Find each white blood cell.
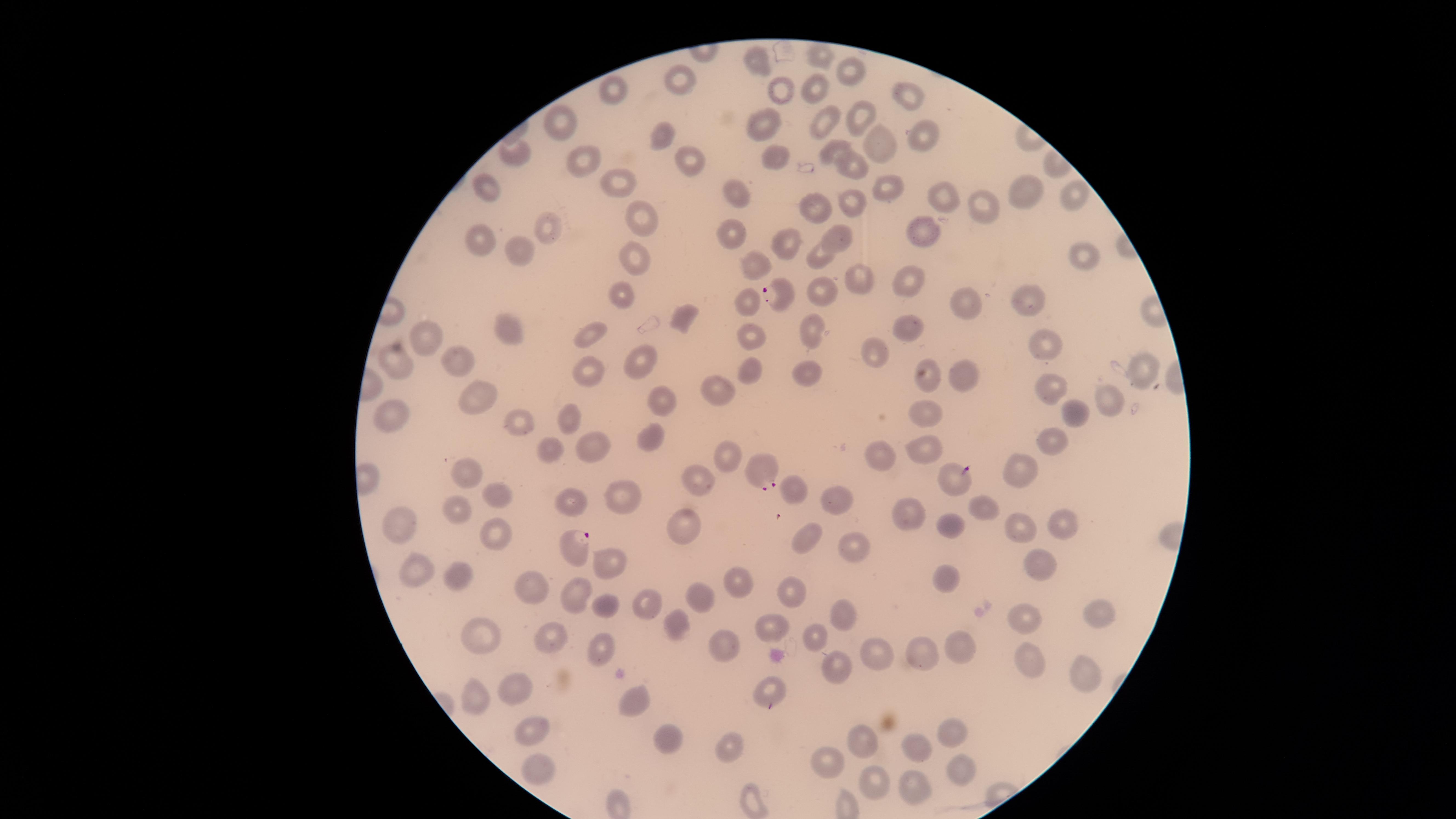
No white blood cells identified.

visible region = circular
species = Plasmodium falciparum
uninfected red blood cells = approximate marker points, in pixels from the top-left corner: (x=817, y=54), (x=759, y=62), (x=848, y=67), (x=682, y=82), (x=818, y=88), (x=613, y=90), (x=777, y=90), (x=910, y=90), (x=861, y=113), (x=567, y=116), (x=825, y=118), (x=768, y=124), (x=661, y=132), (x=922, y=138), (x=877, y=146), (x=831, y=147), (x=520, y=155), (x=772, y=155), (x=576, y=161), (x=686, y=162), (x=846, y=166), (x=610, y=180), (x=483, y=186), (x=890, y=190), (x=1020, y=192), (x=941, y=195), (x=1078, y=196), (x=744, y=201), (x=978, y=203), (x=815, y=204), (x=857, y=204), (x=643, y=216), (x=548, y=226), (x=730, y=230), (x=837, y=236), (x=485, y=238), (x=920, y=241), (x=788, y=244), (x=523, y=249), (x=823, y=254), (x=1080, y=256), (x=632, y=261), (x=758, y=262), (x=861, y=279), (x=906, y=281), (x=823, y=292), (x=624, y=296), (x=1024, y=298), (x=967, y=302), (x=748, y=303), (x=687, y=318), (x=817, y=326), (x=507, y=327), (x=590, y=330), (x=906, y=331), (x=425, y=332), (x=756, y=339), (x=1048, y=347), (x=878, y=351), (x=403, y=358), (x=641, y=359), (x=460, y=362), (x=750, y=365), (x=1143, y=370), (x=810, y=371), (x=594, y=373), (x=932, y=375), (x=963, y=375), (x=1053, y=387), (x=714, y=392), (x=662, y=399), (x=485, y=401), (x=1104, y=401), (x=386, y=413), (x=1074, y=415), (x=927, y=416), (x=569, y=419), (x=517, y=421), (x=656, y=437), (x=1046, y=439), (x=920, y=444), (x=552, y=446), (x=597, y=448), (x=886, y=457), (x=727, y=459), (x=1016, y=471), (x=468, y=475), (x=695, y=479), (x=793, y=485), (x=627, y=489), (x=499, y=493), (x=835, y=499), (x=984, y=506), (x=905, y=509), (x=457, y=511), (x=405, y=520), (x=1067, y=522), (x=688, y=523), (x=947, y=524), (x=1021, y=526), (x=497, y=534), (x=811, y=539), (x=853, y=547), (x=1038, y=561), (x=609, y=562), (x=420, y=571), (x=463, y=571), (x=736, y=582), (x=948, y=585), (x=789, y=586), (x=535, y=591), (x=576, y=595), (x=701, y=595), (x=649, y=599), (x=606, y=602), (x=841, y=613), (x=1099, y=617), (x=1026, y=619), (x=683, y=624), (x=772, y=625), (x=481, y=632), (x=551, y=635), (x=822, y=635), (x=724, y=642), (x=606, y=645), (x=930, y=647), (x=959, y=647), (x=875, y=652), (x=1033, y=666), (x=1087, y=668), (x=838, y=671), (x=523, y=684), (x=768, y=685), (x=471, y=697), (x=635, y=698), (x=534, y=728), (x=954, y=730), (x=667, y=736), (x=863, y=739), (x=918, y=743), (x=726, y=746), (x=832, y=762), (x=959, y=767), (x=540, y=768), (x=869, y=783), (x=913, y=785), (x=752, y=802)
presence = malaria parasites identified
image size = 1456×819 pixels
parasitized red blood cells = approximate marker points, in pixels from the top-left corner: (x=776, y=290), (x=756, y=468), (x=955, y=478), (x=578, y=548)
field of view = single
stain = Giemsa
capture = smartphone photograph through the microscope eyepiece
preparation = thin blood film